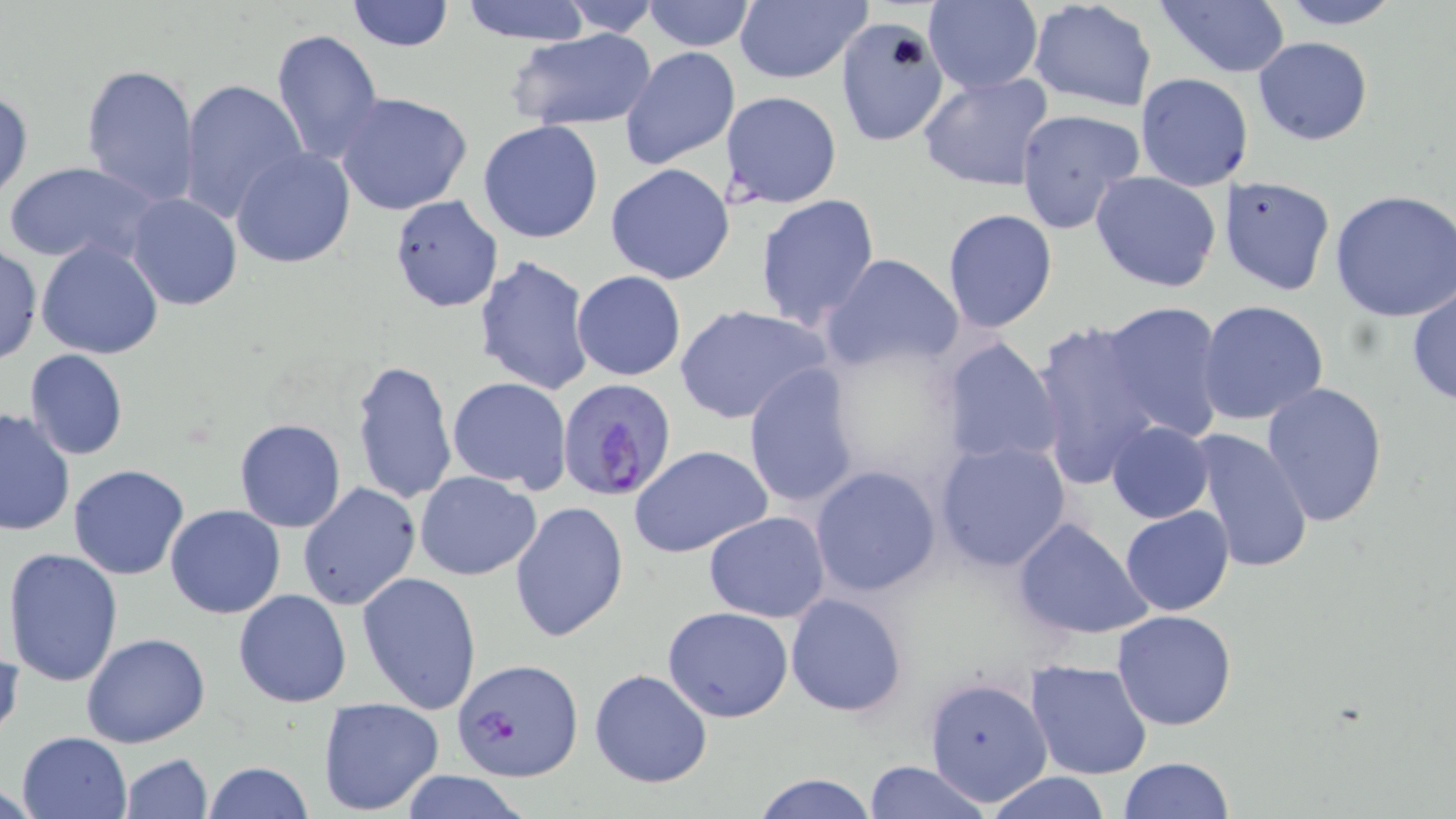
slide_level_diagnosis: Plasmodium falciparum
field_of_view: one of a larger specimen
preparation: thin blood smear
image_size: 1456×819 pixels
uninfected_red_blood_cell_locations: 'approximate bounding boxes as named x1/y1/x2/y2 corners in pixels: (x1=347, y1=0, x2=454, y2=51), (x1=456, y1=0, x2=596, y2=44), (x1=547, y1=0, x2=667, y2=33), (x1=640, y1=0, x2=757, y2=52), (x1=733, y1=0, x2=872, y2=86), (x1=1026, y1=0, x2=1159, y2=113), (x1=1273, y1=0, x2=1407, y2=30), (x1=1156, y1=1, x2=1291, y2=79), (x1=919, y1=4, x2=1044, y2=93), (x1=834, y1=15, x2=951, y2=146), (x1=270, y1=28, x2=383, y2=165), (x1=505, y1=28, x2=657, y2=130), (x1=1252, y1=37, x2=1373, y2=145), (x1=619, y1=46, x2=740, y2=172), (x1=80, y1=62, x2=200, y2=208), (x1=917, y1=70, x2=1056, y2=193), (x1=1136, y1=73, x2=1253, y2=191), (x1=178, y1=79, x2=307, y2=222), (x1=1, y1=88, x2=34, y2=200), (x1=333, y1=91, x2=473, y2=216), (x1=720, y1=91, x2=843, y2=209), (x1=1014, y1=107, x2=1143, y2=234), (x1=478, y1=120, x2=604, y2=244), (x1=231, y1=147, x2=356, y2=268), (x1=6, y1=161, x2=159, y2=267), (x1=604, y1=163, x2=734, y2=284), (x1=1090, y1=171, x2=1222, y2=294), (x1=1220, y1=176, x2=1335, y2=296), (x1=1328, y1=188, x2=1456, y2=322), (x1=128, y1=194, x2=242, y2=310), (x1=389, y1=195, x2=503, y2=313), (x1=754, y1=195, x2=882, y2=330), (x1=941, y1=208, x2=1059, y2=334), (x1=35, y1=240, x2=164, y2=359), (x1=0, y1=244, x2=43, y2=365), (x1=821, y1=252, x2=964, y2=373), (x1=473, y1=254, x2=595, y2=396), (x1=572, y1=269, x2=687, y2=381), (x1=1406, y1=285, x2=1455, y2=407), (x1=1196, y1=300, x2=1330, y2=426), (x1=1098, y1=301, x2=1228, y2=443), (x1=674, y1=304, x2=833, y2=426), (x1=1030, y1=318, x2=1169, y2=489), (x1=939, y1=335, x2=1064, y2=471), (x1=24, y1=349, x2=128, y2=461), (x1=351, y1=358, x2=458, y2=506), (x1=741, y1=364, x2=863, y2=511), (x1=447, y1=377, x2=571, y2=494), (x1=1260, y1=381, x2=1389, y2=527), (x1=0, y1=405, x2=75, y2=537), (x1=233, y1=419, x2=346, y2=533), (x1=1107, y1=421, x2=1214, y2=524), (x1=1188, y1=426, x2=1314, y2=575), (x1=934, y1=439, x2=1071, y2=572), (x1=628, y1=444, x2=774, y2=561), (x1=68, y1=464, x2=189, y2=580), (x1=809, y1=465, x2=942, y2=597), (x1=416, y1=471, x2=541, y2=579), (x1=297, y1=483, x2=420, y2=612), (x1=509, y1=502, x2=629, y2=641), (x1=165, y1=504, x2=287, y2=619), (x1=1121, y1=505, x2=1234, y2=615), (x1=703, y1=511, x2=831, y2=624), (x1=1012, y1=518, x2=1153, y2=639), (x1=3, y1=546, x2=125, y2=687), (x1=357, y1=572, x2=482, y2=716), (x1=233, y1=588, x2=352, y2=708), (x1=785, y1=593, x2=907, y2=717), (x1=662, y1=607, x2=794, y2=721), (x1=1112, y1=609, x2=1238, y2=731), (x1=81, y1=633, x2=210, y2=749), (x1=1, y1=638, x2=22, y2=747), (x1=1023, y1=659, x2=1153, y2=781), (x1=588, y1=668, x2=713, y2=789), (x1=922, y1=676, x2=1053, y2=808), (x1=317, y1=697, x2=445, y2=816), (x1=16, y1=730, x2=134, y2=819), (x1=121, y1=753, x2=213, y2=819), (x1=1119, y1=757, x2=1235, y2=818), (x1=863, y1=760, x2=988, y2=819), (x1=202, y1=762, x2=315, y2=819), (x1=395, y1=771, x2=531, y2=819), (x1=983, y1=772, x2=1111, y2=819), (x1=753, y1=773, x2=878, y2=818)'
stain: May-Grünwald-Giemsa
modality: light microscopy
plasmodium_falciparum_infected_red_blood_cell_locations: 'approximate bounding boxes as named x1/y1/x2/y2 corners in pixels: (x1=555, y1=377, x2=678, y2=504), (x1=452, y1=656, x2=582, y2=782)'
magnification: 1000x